Describe the morphology of the erythrocytes.
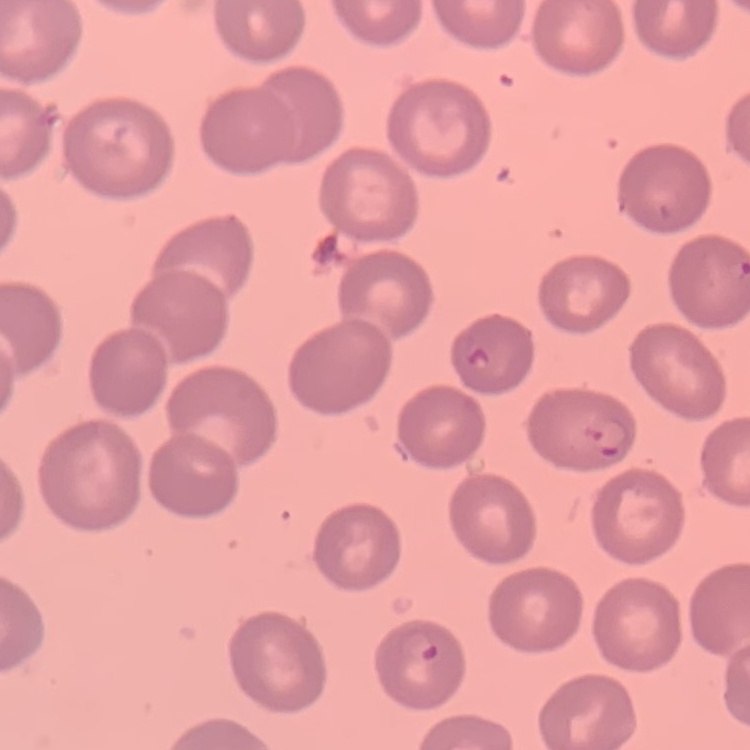
They show no rouleaux formation.

stain: Field's or Giemsa
preparation: thin blood film
image_type: one tile cut from a larger photomicrograph